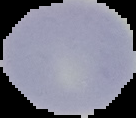
{
  "image_type": "segmented cell region with the area outside set to black",
  "malaria_status": "uninfected",
  "preparation": "thin blood film",
  "image_size": "136×118 pixels"
}